Point out each leukocyte.
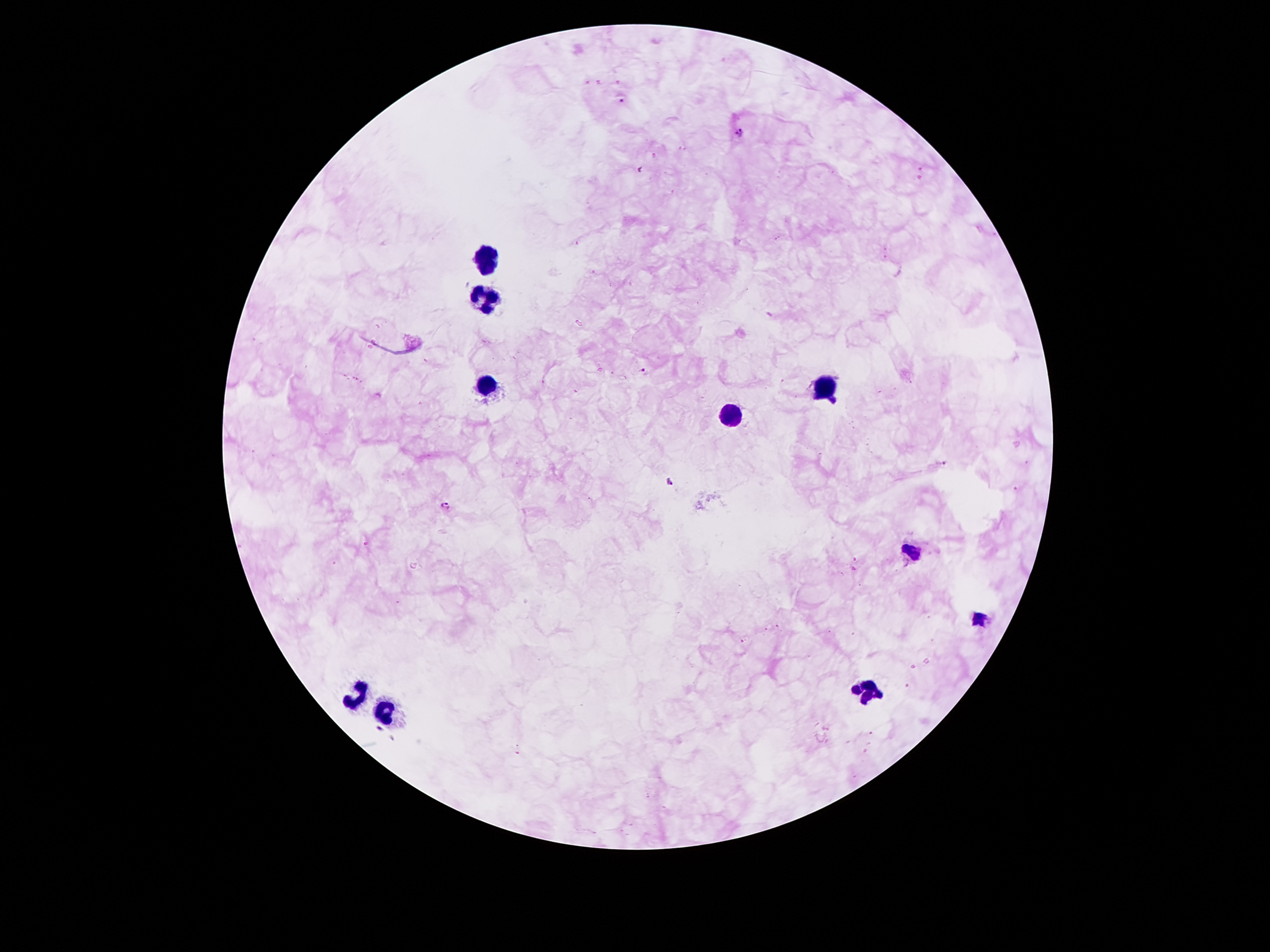
Approximate object centers, in pixels from the top-left corner.
Leukocytes: (x=484, y=255), (x=484, y=293), (x=489, y=383), (x=828, y=391), (x=733, y=413), (x=915, y=553), (x=982, y=620), (x=870, y=689), (x=358, y=694), (x=386, y=707).

Summary:
  - Plasmodium parasite locations: (x=622, y=102), (x=741, y=132), (x=644, y=373), (x=947, y=464), (x=670, y=482), (x=445, y=506), (x=380, y=728)
  - Capture: smartphone camera through the microscope eyepiece
  - Magnification: 100x
  - Image size: 1270×952 pixels
  - Stain: Giemsa
  - Patient malaria status: infected with Plasmodium falciparum
  - Preparation: thick peripheral-blood smear
  - Field of view: single